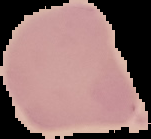 Result: no malaria parasites seen. Image is 151×139 pixels. From a thin blood smear. Segmented cell region on a black background.